Name the blood parasite species.
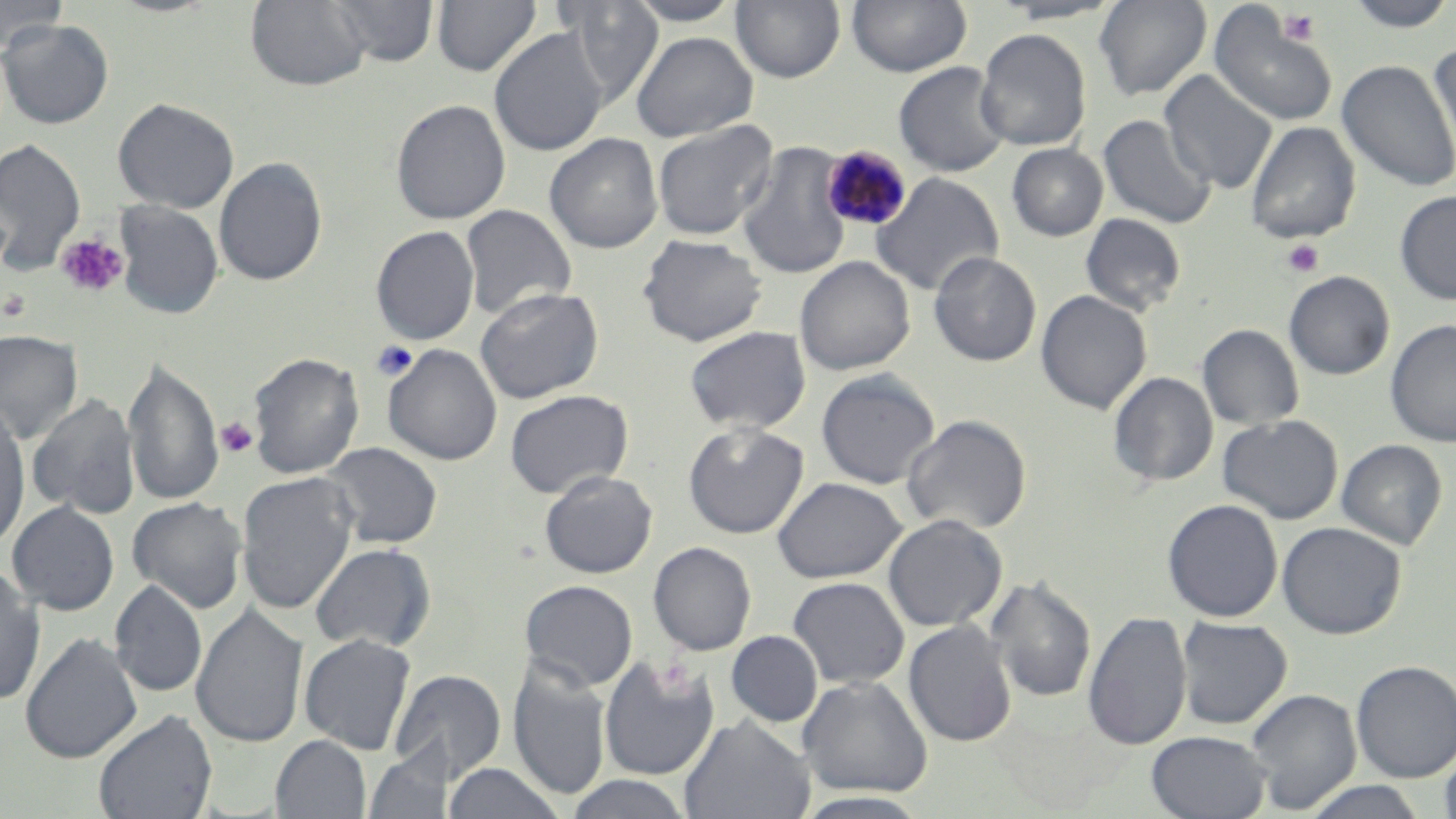
Plasmodium malariae.

Approximate bounding boxes as (x1, y1, x2, y2) in pixels. Plasmodium malariae-infected red blood cell locations: (821, 144, 914, 231). Platelet locations: (1277, 8, 1322, 46), (56, 232, 129, 298), (1282, 239, 1325, 277), (1, 289, 31, 322), (216, 417, 259, 459). Uninfected red blood cell locations: (0, 0, 70, 55), (246, 0, 372, 92), (330, 0, 439, 67), (624, 0, 743, 26), (731, 0, 845, 83), (847, 0, 972, 76), (1093, 0, 1212, 100), (1343, 0, 1456, 32), (431, 1, 541, 76), (556, 1, 666, 104), (989, 1, 1126, 25), (1209, 6, 1338, 127), (0, 19, 114, 129), (489, 28, 609, 157), (975, 28, 1092, 151), (630, 31, 758, 142), (1428, 42, 1456, 166), (1337, 58, 1456, 192), (893, 61, 1010, 177), (1160, 71, 1278, 193), (112, 97, 239, 213), (391, 98, 511, 225), (1098, 114, 1217, 230), (652, 120, 777, 240), (1246, 121, 1360, 243), (544, 133, 663, 253), (0, 137, 86, 274), (736, 141, 853, 280), (1006, 143, 1108, 242), (213, 157, 328, 287), (870, 171, 1004, 297), (1394, 190, 1456, 304), (113, 200, 224, 319), (460, 204, 577, 321), (1080, 212, 1187, 316), (370, 225, 479, 345), (637, 234, 768, 347), (929, 251, 1042, 366), (794, 256, 915, 376), (1284, 271, 1394, 380), (474, 286, 604, 404), (1035, 290, 1152, 415), (1385, 319, 1456, 447), (1197, 324, 1304, 430), (684, 325, 811, 433), (0, 329, 83, 444), (383, 343, 503, 466), (248, 351, 365, 478), (123, 357, 223, 509), (816, 370, 940, 490), (1108, 371, 1218, 487), (504, 389, 633, 498), (28, 393, 141, 520), (0, 404, 31, 552), (900, 414, 1032, 535), (1217, 414, 1344, 524), (682, 422, 809, 539), (1336, 439, 1447, 551), (320, 442, 443, 549), (539, 470, 657, 578), (237, 472, 358, 616), (772, 476, 907, 584), (127, 497, 247, 613), (1162, 499, 1283, 622), (7, 501, 120, 616), (883, 514, 1006, 631), (1277, 521, 1406, 639), (648, 541, 756, 655), (310, 542, 436, 653), (0, 565, 46, 705), (985, 575, 1097, 704), (787, 577, 910, 689), (520, 579, 638, 691), (110, 580, 207, 699), (191, 603, 309, 749), (1083, 611, 1191, 750), (1175, 616, 1292, 729), (903, 620, 1017, 747), (726, 630, 823, 727), (20, 632, 142, 763), (299, 633, 416, 755), (599, 655, 721, 781), (1351, 660, 1456, 782), (508, 662, 611, 801), (389, 668, 507, 783), (797, 675, 933, 798), (1245, 688, 1362, 814), (92, 709, 218, 819), (679, 715, 815, 818), (1146, 730, 1271, 818), (270, 735, 371, 819), (1439, 743, 1456, 819), (364, 748, 444, 819), (445, 762, 566, 819), (562, 774, 694, 818), (1300, 780, 1429, 819), (793, 791, 933, 817). Light microscopy. Image is 1456×819 pixels. May-Grünwald-Giemsa-stained preparation. Single field of view. Thin blood film. Captured at 1000x magnification.